Assess this cell for malaria.
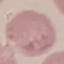

Uninfected.

preparation = thin blood smear
capture = smartphone camera at the microscope eyepiece
stain = Giemsa
image type = cell patch, automatically extracted from a larger field of view and resized to 64 × 64 pixels